Identify the cell.
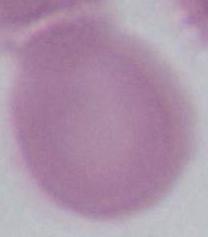

An erythrocyte.

1000x magnification. Micrograph.